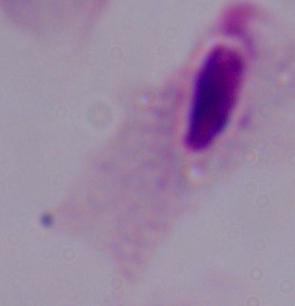
identification = trichomonad
magnification = 1000x
modality = micrograph